Identify the preparation type.
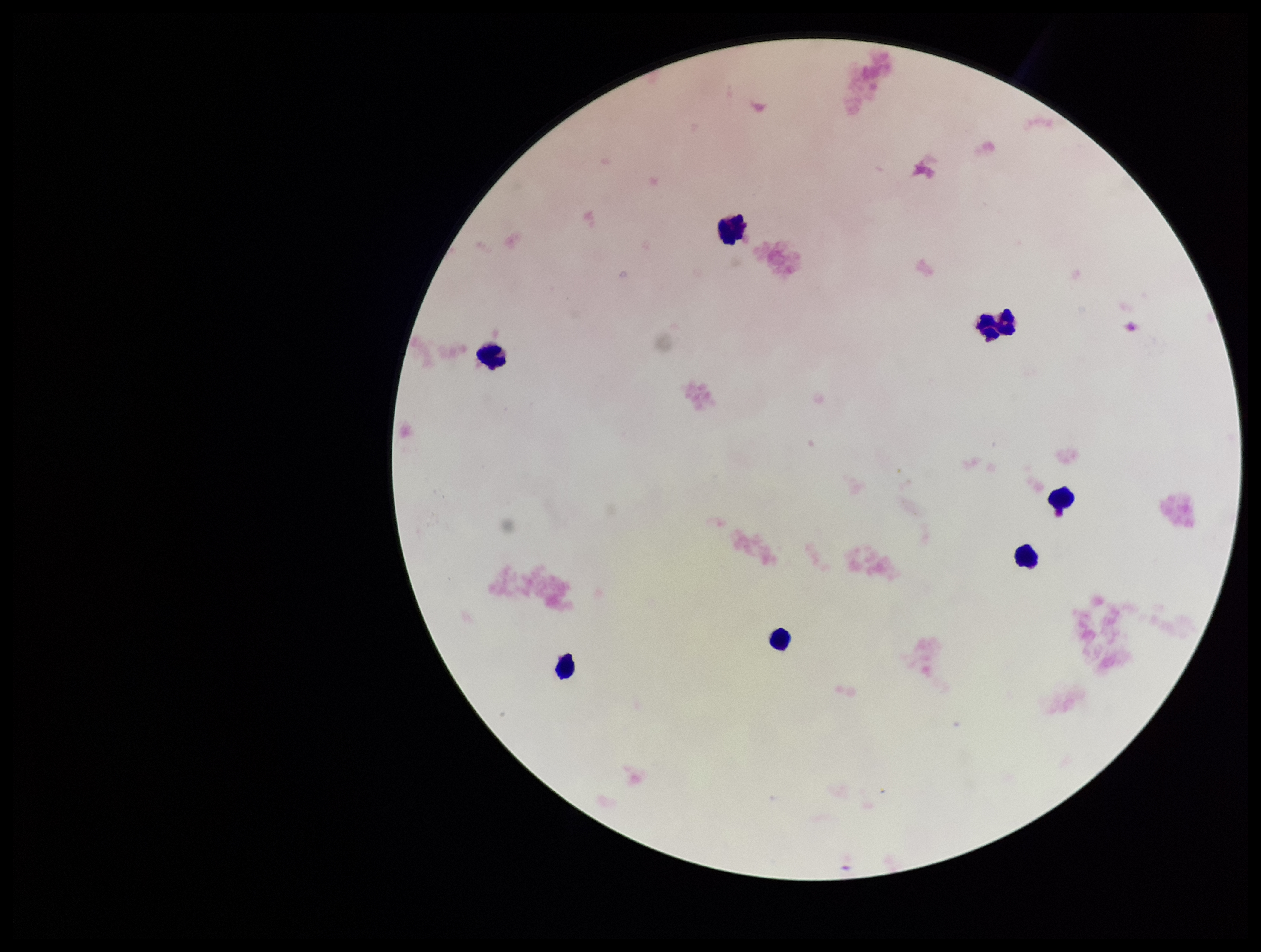

Thick.

Stained with Giemsa. Image is 1261×952 pixels. Patient malaria status: negative. Parasite count: 0. Photographed through the microscope eyepiece with a smartphone camera. Leukocyte count: 7. Plasmodium parasites: none identified. Single field of view.